Assess this cell for malaria.
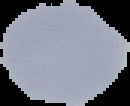

It is uninfected.

preparation: thin blood smear
image_size: 130×106 pixels
image_type: segmented cell region with the area outside set to black